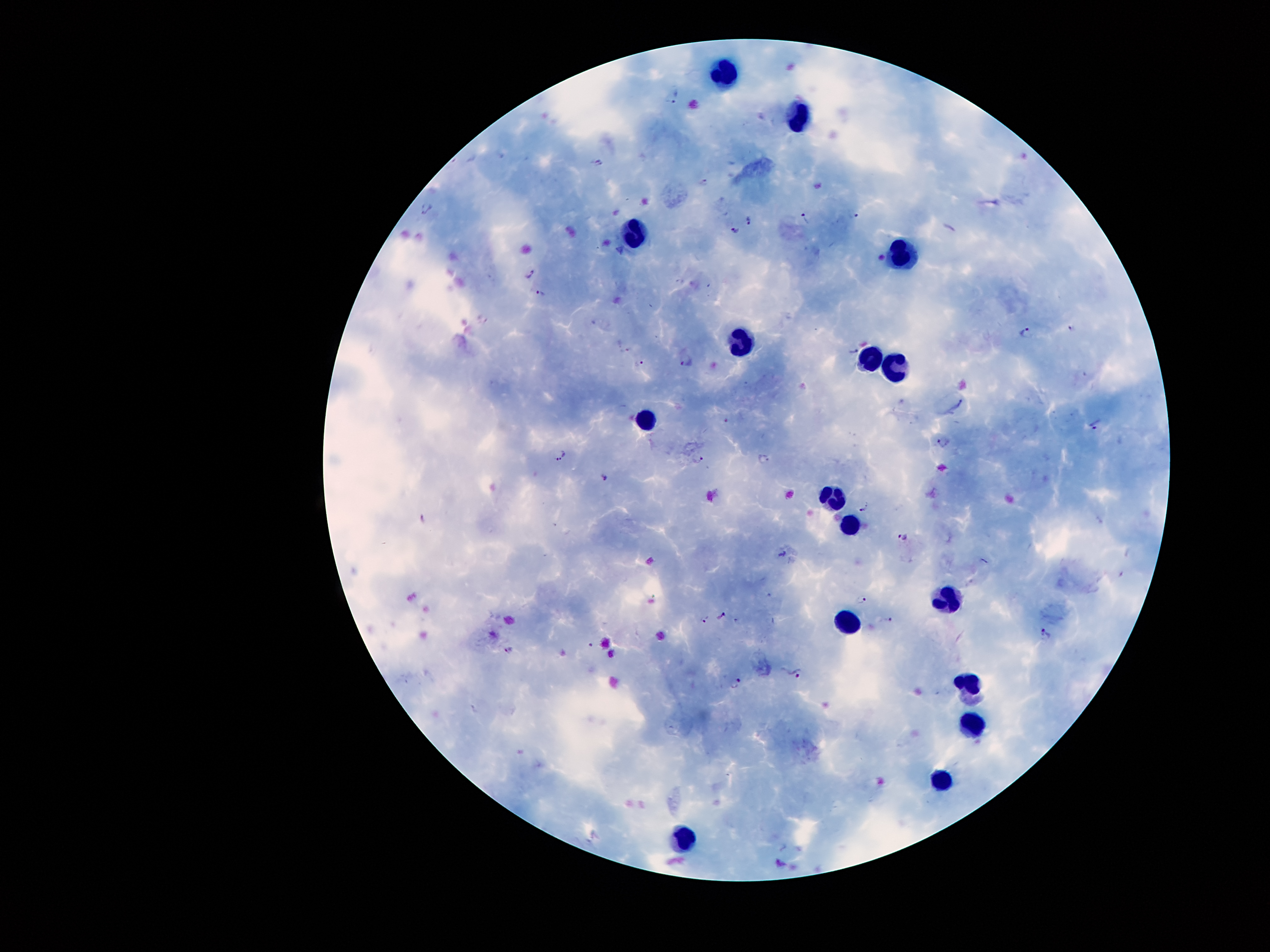
Approximate centers as (x, y) in pixels. Leukocyte locations: (725, 78), (797, 112), (637, 235), (899, 245), (744, 346), (864, 357), (901, 372), (647, 420), (830, 494), (844, 524), (944, 598), (847, 620), (968, 682), (978, 722), (944, 778), (681, 836). Malaria parasite locations: (676, 99), (601, 163), (705, 183), (857, 214), (749, 218), (805, 219), (732, 232), (882, 258), (530, 274), (541, 291), (1073, 327), (1027, 332), (628, 349), (853, 350), (687, 361), (641, 363), (1095, 423), (943, 443), (561, 454), (698, 458), (764, 458), (604, 479), (864, 509), (422, 518), (903, 538), (785, 554), (864, 596), (722, 617), (889, 618), (706, 621), (1045, 633), (507, 650), (797, 673), (737, 684). Patient malaria status: positive for Plasmodium falciparum. 100x magnification. Thick peripheral-blood smear. Giemsa-stained preparation. Image is 1270×952 pixels. Photographed through the microscope eyepiece with a smartphone camera. Single field of view.